Identify the preparation type.
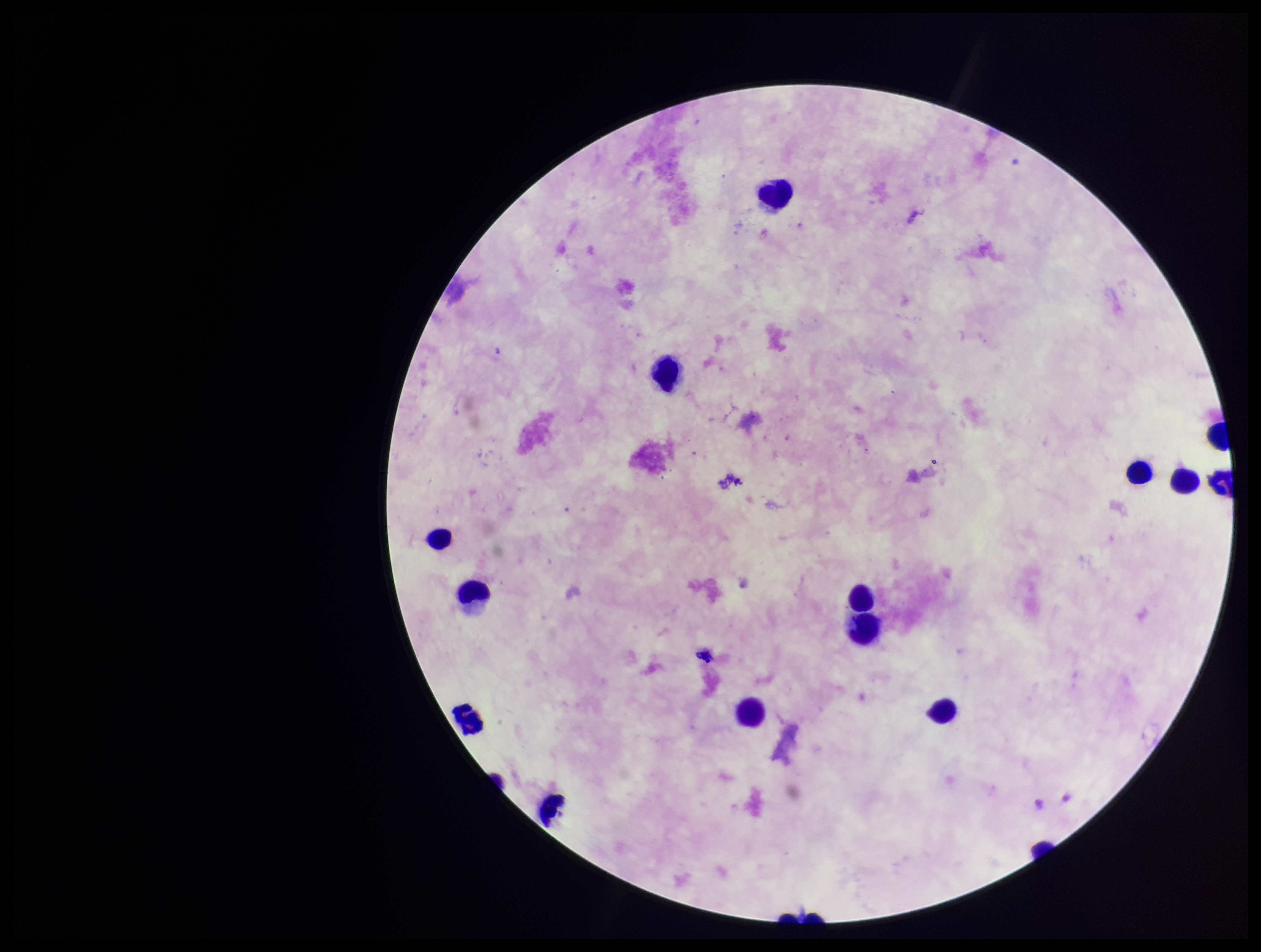

A thick smear.

Summary:
  - Image size: 1261×952 pixels
  - Patient malaria status: negative
  - Parasite count: 0
  - Field of view: single
  - Stain: Giemsa
  - Plasmodium parasites: none identified
  - Leukocyte count: 16
  - Capture: smartphone photograph through the microscope eyepiece